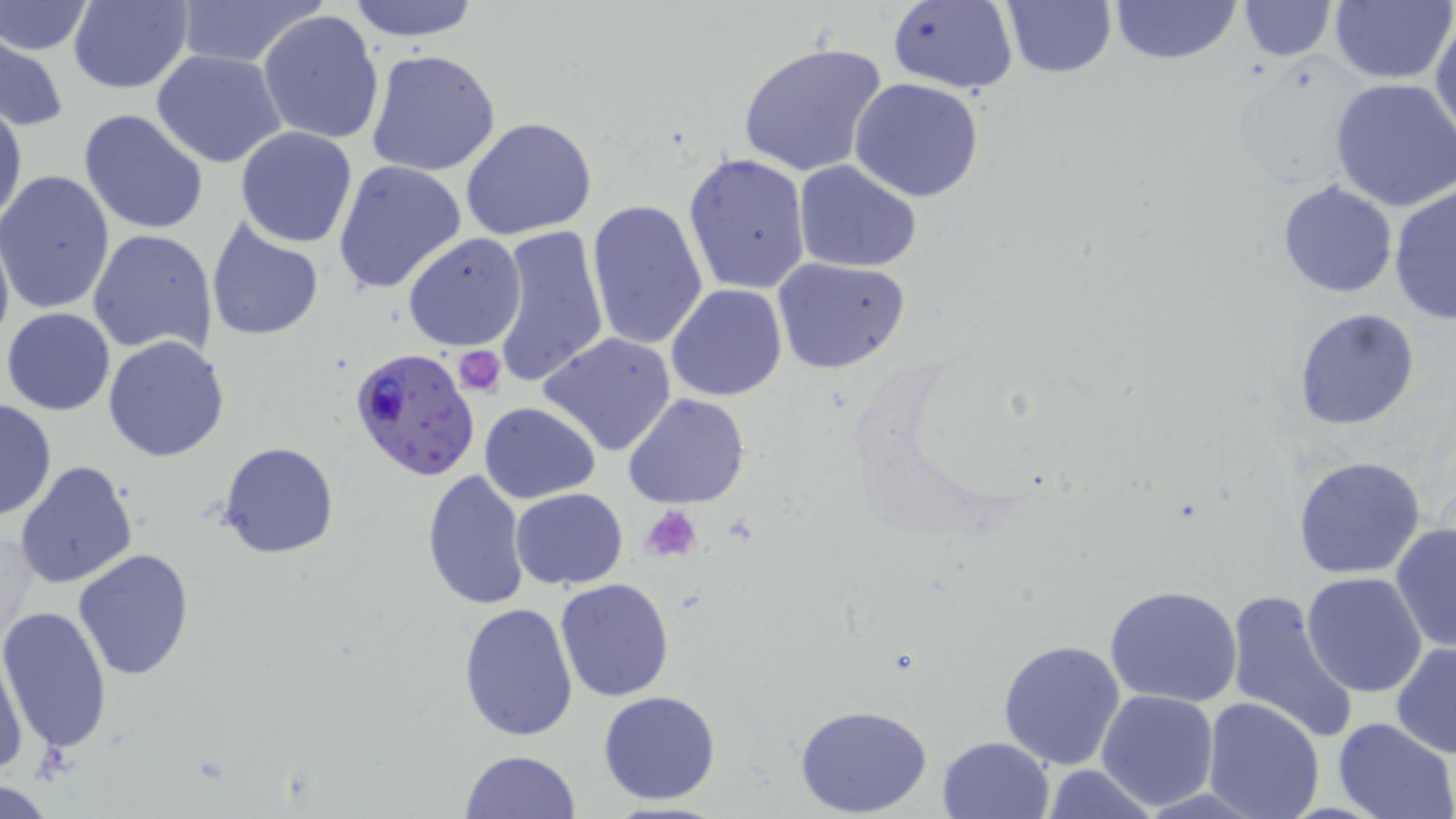

slide-level diagnosis = Plasmodium falciparum
stain = May-Grünwald-Giemsa
uninfected red blood cell locations = approximate bounding boxes as (x1,y1)-(x2,y2) corner pairs in pixels: (168,0)-(329,68), (346,0)-(480,43), (886,0)-(1018,93), (1002,0)-(1117,78), (1106,0)-(1242,65), (1237,0)-(1336,60), (1330,0)-(1456,84), (1,1)-(94,56), (65,1)-(195,93), (258,9)-(385,146), (1433,10)-(1456,147), (1,37)-(70,133), (738,41)-(890,180), (151,49)-(288,169), (364,49)-(503,178), (1229,70)-(1362,192), (848,78)-(987,203), (1331,79)-(1456,213), (0,100)-(27,233), (78,109)-(210,236), (462,116)-(597,242), (236,126)-(358,247), (684,153)-(811,295), (332,159)-(465,295), (795,160)-(922,272), (0,171)-(115,314), (1277,180)-(1398,298), (1389,184)-(1456,327), (586,198)-(709,352), (205,216)-(325,339), (0,218)-(14,358), (486,223)-(611,391), (86,228)-(218,357), (402,234)-(527,350), (770,255)-(911,375), (667,284)-(786,401), (2,306)-(115,416), (1294,307)-(1421,431), (537,332)-(678,458), (104,334)-(232,462), (623,393)-(750,511), (0,397)-(57,522), (479,402)-(600,503), (217,440)-(339,560), (1293,455)-(1427,579), (13,460)-(140,590), (420,467)-(530,610), (510,488)-(627,590), (1390,522)-(1455,653), (73,549)-(196,681), (1302,572)-(1430,697), (555,577)-(674,702), (1105,583)-(1244,706), (1225,587)-(1359,743), (458,601)-(579,742), (0,605)-(112,755), (6,628)-(50,776), (997,639)-(1127,772), (1391,639)-(1456,758), (1,644)-(27,776), (1096,689)-(1218,808), (597,690)-(722,806), (1203,697)-(1326,819), (792,703)-(934,817), (1331,718)-(1456,819), (936,736)-(1054,819), (460,748)-(581,818), (1041,764)-(1163,818), (1,780)-(59,816)
field of view = one of a larger specimen
platelet locations = approximate bounding boxes as (x1,y1)-(x2,y2) corner pairs in pixels: (454,345)-(507,395), (641,506)-(704,561)
image size = 1456×819 pixels
magnification = 1000x
preparation = thin blood film
modality = light microscopy
Plasmodium falciparum-infected red blood cell locations = approximate bounding boxes as (x1,y1)-(x2,y2) corner pairs in pixels: (349,346)-(481,482)